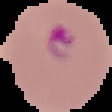

Image is 112×112 pixels. From a thin blood film. Segmented cell region on a black background. Malaria status: parasitized.